Name the parasite shown.
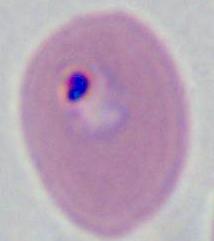

This is Plasmodium.

Summary:
  - Magnification: 400x or 1000x
  - Modality: micrograph